Give the extent of all Plasmodium ovale-infected red blood cells.
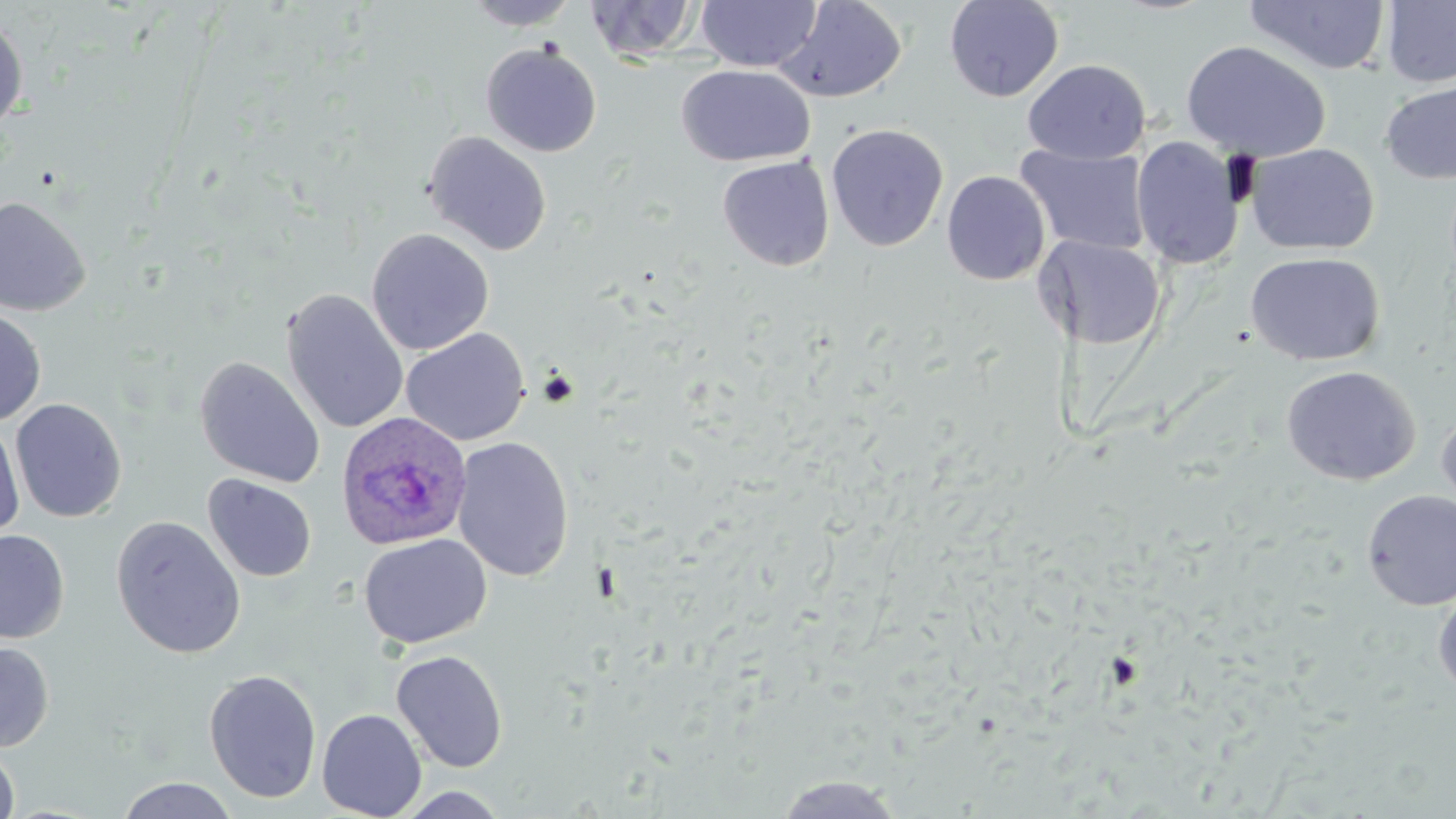
Approximate bounding boxes as [x1, y1, x2, y2] in pixels.
Plasmodium ovale-infected red blood cells: [335, 411, 473, 551].

Uninfected red blood cell locations: [463, 0, 581, 30], [584, 0, 703, 63], [695, 0, 822, 71], [944, 0, 1064, 102], [1243, 0, 1391, 76], [774, 1, 908, 104], [1381, 1, 1456, 88], [0, 14, 29, 135], [1181, 40, 1330, 162], [481, 43, 602, 157], [1023, 59, 1151, 164], [677, 64, 816, 166], [1380, 79, 1456, 185], [825, 123, 949, 253], [422, 131, 552, 256], [1131, 136, 1245, 269], [1247, 143, 1379, 255], [1015, 145, 1152, 256], [717, 156, 835, 271], [942, 170, 1050, 285], [0, 195, 93, 316], [366, 228, 495, 355], [1037, 236, 1166, 350], [1245, 252, 1385, 366], [282, 288, 409, 434], [0, 306, 46, 426], [401, 328, 530, 446], [194, 356, 325, 488], [1281, 366, 1420, 485], [10, 397, 127, 523], [1437, 403, 1456, 524], [0, 418, 25, 541], [452, 436, 575, 581], [203, 473, 317, 583], [1361, 489, 1456, 610], [110, 515, 247, 658], [0, 529, 69, 644], [359, 534, 492, 650], [1433, 588, 1456, 700], [0, 640, 54, 752], [390, 649, 509, 773], [204, 668, 322, 803], [316, 708, 427, 819], [0, 742, 20, 819], [771, 774, 908, 818], [114, 777, 241, 819], [392, 786, 512, 818]. Slide-level diagnosis: Plasmodium ovale. Captured at 1000x magnification. Image is 1456×819 pixels. May-Grünwald-Giemsa stain. One field of a larger specimen. Optical microscopy. Thin blood smear.